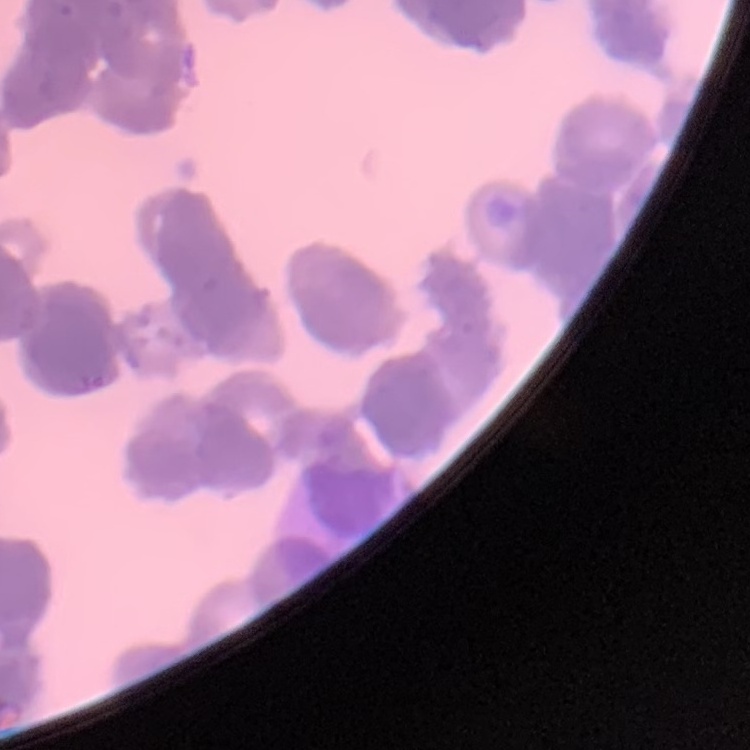

erythrocyte morphology = rouleaux formation
image type = one tile cut from a larger photomicrograph
stain = Field's or Giemsa
preparation = thin blood smear